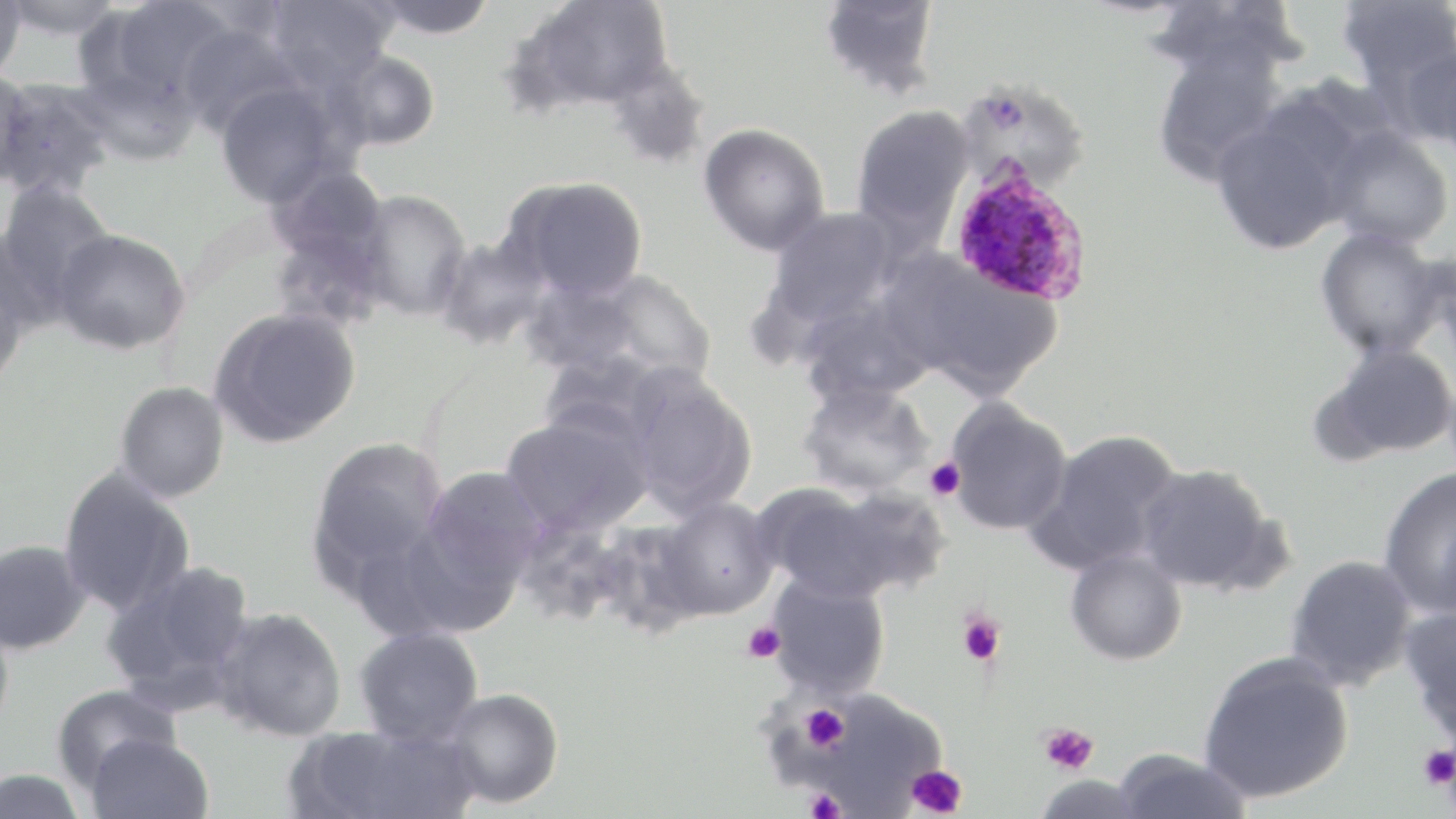
Approximate bounding boxes as (x1, y1, x2, y2) in pixels. Plasmodium ovale-infected red blood cell locations: (948, 165, 1094, 306). Uninfected red blood cell locations: (0, 0, 28, 82), (0, 0, 125, 41), (95, 0, 237, 107), (263, 0, 398, 90), (366, 0, 501, 39), (511, 0, 675, 115), (816, 0, 944, 100), (1336, 0, 1456, 92), (1145, 2, 1307, 86), (176, 23, 305, 139), (1400, 38, 1456, 157), (1149, 42, 1290, 186), (329, 48, 441, 151), (603, 55, 713, 171), (71, 59, 203, 166), (0, 68, 34, 185), (0, 76, 116, 199), (957, 78, 1092, 192), (214, 80, 349, 208), (1210, 99, 1364, 256), (849, 104, 976, 246), (698, 123, 830, 255), (1322, 125, 1454, 249), (264, 163, 390, 273), (500, 175, 649, 301), (0, 181, 116, 314), (353, 189, 472, 322), (765, 206, 899, 327), (1314, 227, 1449, 360), (52, 228, 191, 356), (432, 235, 553, 351), (1422, 243, 1456, 363), (0, 244, 35, 388), (888, 251, 1064, 399), (583, 270, 719, 386), (516, 274, 648, 381), (799, 295, 934, 407), (208, 306, 361, 448), (1320, 341, 1456, 461), (620, 367, 758, 521), (114, 380, 230, 502), (797, 381, 935, 498), (944, 398, 1073, 536), (500, 413, 653, 536), (1026, 429, 1183, 575), (307, 435, 450, 593), (1134, 463, 1277, 595), (1378, 465, 1456, 619), (58, 466, 197, 617), (419, 466, 547, 598), (753, 483, 912, 602), (652, 496, 778, 621), (513, 516, 634, 627), (0, 538, 92, 655), (1065, 547, 1188, 666), (1283, 554, 1419, 691), (101, 560, 257, 714), (765, 572, 891, 700), (1400, 606, 1456, 744), (212, 607, 347, 742), (354, 625, 484, 745), (1198, 650, 1354, 805), (52, 685, 180, 789), (442, 687, 564, 809), (805, 690, 946, 814), (292, 721, 480, 819), (85, 733, 214, 819), (1111, 748, 1253, 819), (0, 767, 89, 819), (1032, 774, 1149, 817). Platelet locations: (923, 457, 965, 501), (957, 609, 1007, 667), (742, 621, 785, 663), (801, 705, 849, 752), (1038, 721, 1098, 775), (1418, 743, 1456, 790), (905, 764, 968, 818), (804, 788, 846, 819). Slide-level diagnosis: Plasmodium ovale. Thin blood film. Image is 1456×819 pixels. Light microscopy. 1000x magnification. May-Grünwald-Giemsa-stained preparation. One field of a larger specimen.